Describe the morphology of the red blood cells.
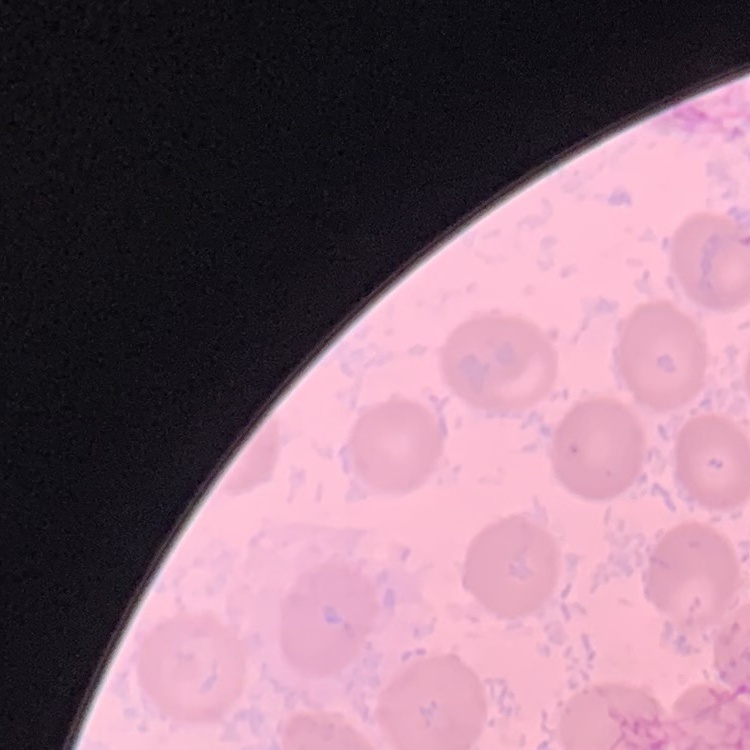
No rouleaux formation.

Summary:
  - Stain: Field's or Giemsa
  - Image type: square crop of a larger photomicrograph
  - Preparation: thin blood smear